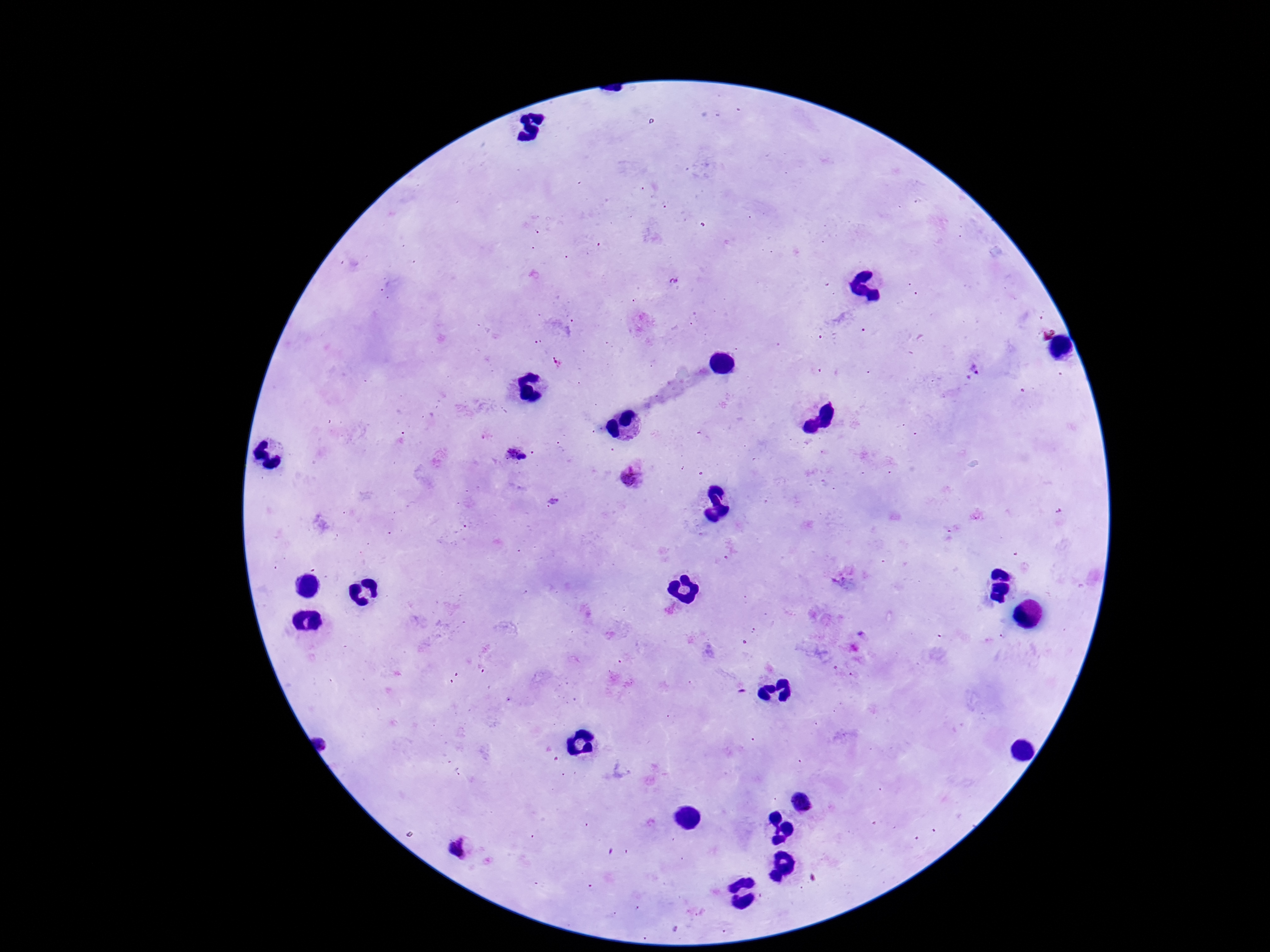
Approximate object centers, in pixels from the top-left corner.
Summary:
  - Plasmodium parasite locations: (x=976, y=368), (x=632, y=475), (x=459, y=849)
  - Patient malaria status: infected
  - Preparation: thick blood film
  - Image size: 1270×952 pixels
  - Magnification: 100x
  - Stain: Giemsa
  - Capture: smartphone camera through the microscope eyepiece
  - Field of view: one from this slide